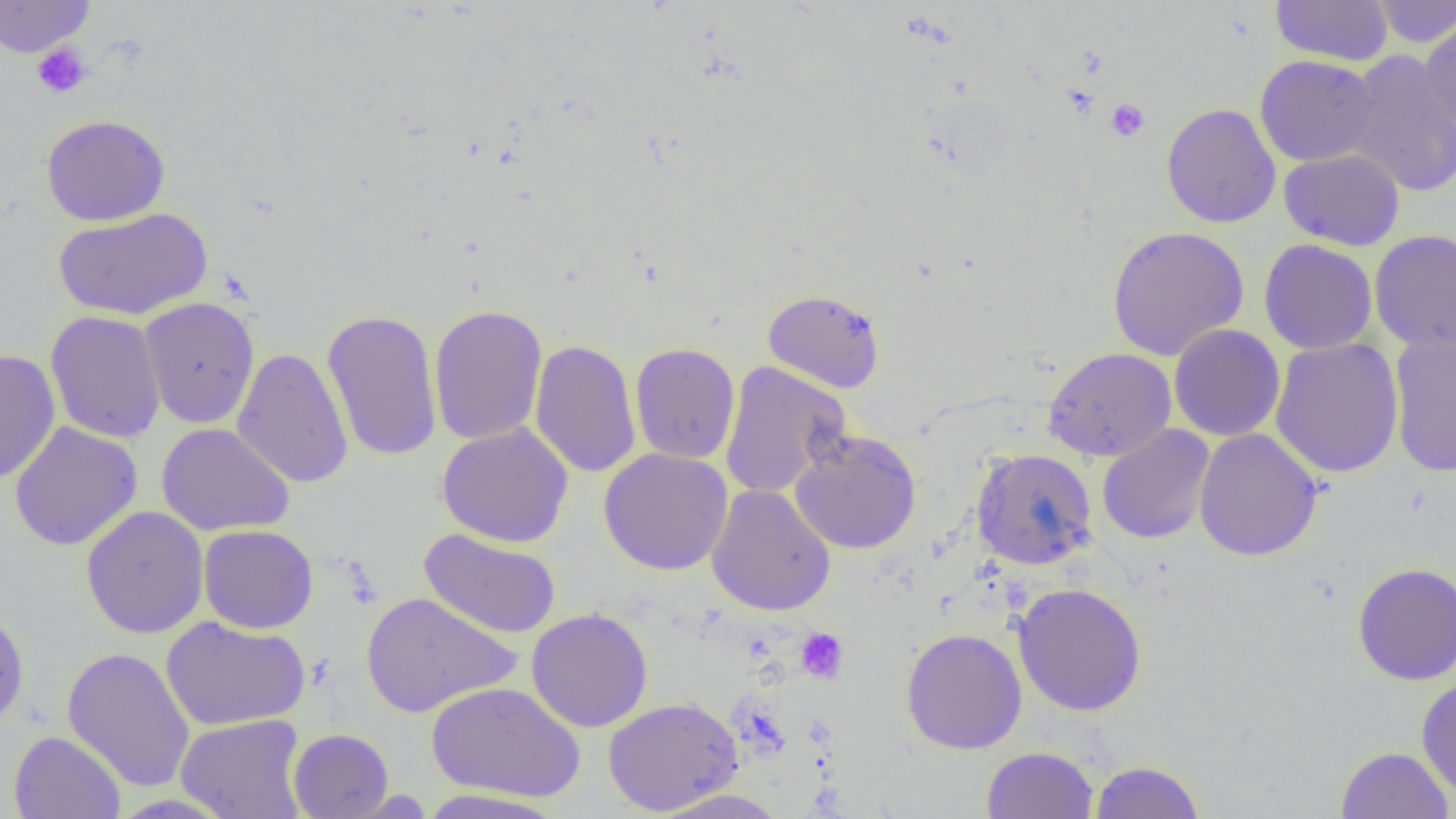
slide-level diagnosis = negative for blood parasites
platelet locations = approximate bounding boxes as (x1,y1)-(x2,y2) corner pairs in pixels: (32,42)-(93,98), (1106,98)-(1149,142), (795,628)-(848,683)
modality = light microscopy
uninfected red blood cell locations = approximate bounding boxes as (x1,y1)-(x2,y2) corner pairs in pixels: (0,0)-(95,58), (1270,0)-(1393,66), (1369,0)-(1456,48), (1420,17)-(1456,138), (1343,49)-(1456,198), (1255,55)-(1380,167), (1160,102)-(1281,229), (41,114)-(171,226), (1278,149)-(1405,251), (53,207)-(212,321), (1107,225)-(1249,361), (1369,229)-(1456,353), (1259,239)-(1378,355), (762,288)-(885,394), (139,297)-(260,429), (429,303)-(548,446), (321,308)-(443,463), (45,311)-(167,444), (1169,324)-(1285,442), (1388,332)-(1456,477), (1269,337)-(1404,478), (529,339)-(642,479), (630,342)-(740,464), (232,347)-(354,489), (1042,347)-(1177,463), (0,350)-(61,485), (719,361)-(851,499), (9,422)-(143,550), (157,422)-(294,536), (437,422)-(574,547), (1097,423)-(1215,544), (1193,428)-(1323,562), (789,430)-(921,555), (598,447)-(734,576), (971,447)-(1098,570), (706,484)-(835,616), (81,505)-(209,638), (198,525)-(318,633), (419,528)-(562,639), (1353,562)-(1456,685), (1013,582)-(1147,716), (361,591)-(522,718), (0,608)-(30,733), (526,608)-(653,732), (161,616)-(310,731), (901,628)-(1027,754), (62,647)-(196,792), (1416,673)-(1456,799), (426,681)-(586,802), (603,697)-(742,816), (175,714)-(308,819), (288,728)-(394,818), (9,730)-(125,819), (981,746)-(1099,819), (1335,746)-(1454,819), (1090,760)-(1205,818), (416,788)-(566,818), (650,788)-(792,819)
image size = 1456×819 pixels
preparation = thin blood film
field of view = single
magnification = 1000x